Identify the preparation type.
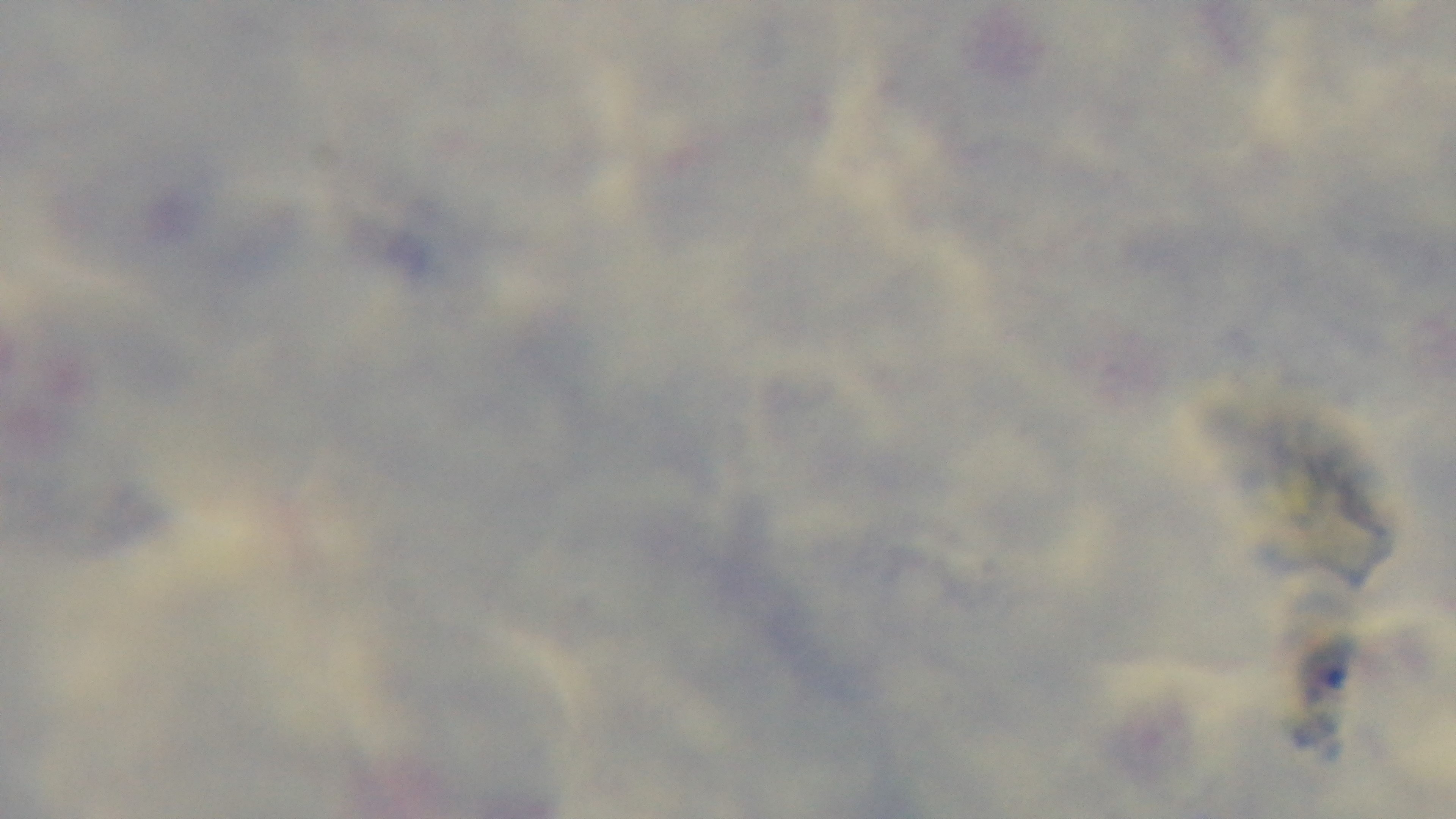

A thick smear.

field of view = single
capture = mounted 4K digital camera
malaria status = uninfected
objective = 100x oil immersion
modality = light microscopy
stain = Giemsa